Classify this cell by malaria status.
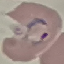
Parasitized.

Giemsa-stained preparation. Thin blood film. Automatically extracted cell patch, resized to 64 × 64 pixels. Photographed with a smartphone camera at the microscope eyepiece.